Classify this cell by malaria status.
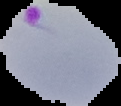

It is parasitized.

Summary:
  - Image size: 121×106 pixels
  - Image type: cell region segmented out of the field of view; surrounding area masked to black
  - Preparation: thin blood film